Name the parasite shown.
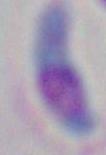

Toxoplasma gondii.

Photomicrograph. Captured at 1000x magnification.